Comment on the morphology of the red blood cells.
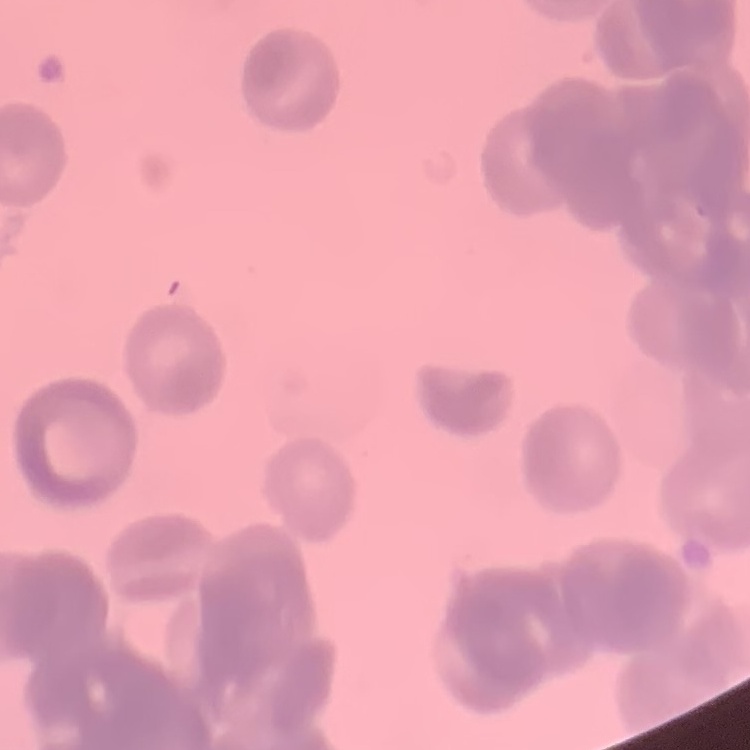
They show rouleaux formation.

Summary:
  - Stain: Field's or Giemsa
  - Preparation: thin peripheral smear
  - Image type: one tile cut from a larger photomicrograph